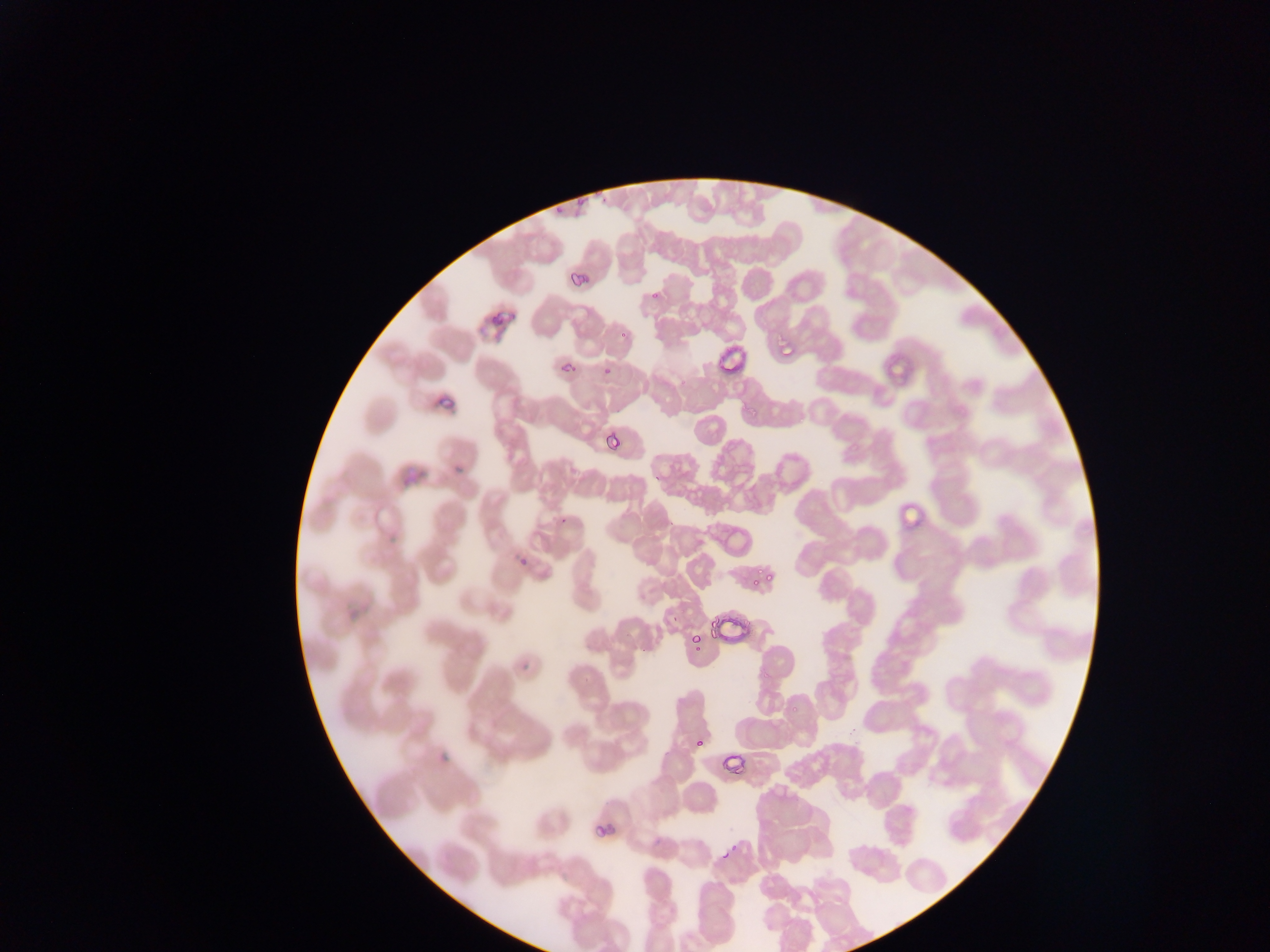
preparation = thin blood smear
country = Ghana
image size = 1270×952 pixels
malaria parasite locations = approximate bounding boxes as [left, top, right, bottom] in pixels: [576, 191, 593, 206], [565, 270, 588, 287], [648, 288, 663, 302], [481, 301, 514, 328], [776, 339, 799, 359], [558, 350, 576, 373], [601, 354, 619, 371], [428, 391, 457, 418], [599, 421, 627, 452], [383, 454, 426, 488], [449, 457, 471, 479], [562, 510, 576, 529], [516, 549, 531, 568], [749, 564, 773, 594], [703, 616, 741, 642], [690, 633, 705, 652], [515, 647, 541, 677], [685, 737, 711, 754], [720, 756, 743, 781], [593, 824, 616, 845], [723, 848, 737, 861]
capture = mobile-phone photograph through a microscope
field of view = single